Classify this cell by malaria status.
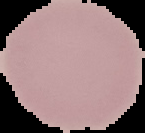

Uninfected.

image size = 145×133 pixels
preparation = thin blood smear
image type = segmented cell region with the area outside set to black